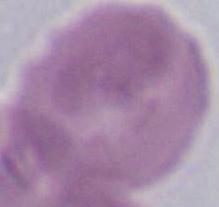
Summary:
  - Modality: micrograph
  - Magnification: 1000x
  - Identification: red blood cell